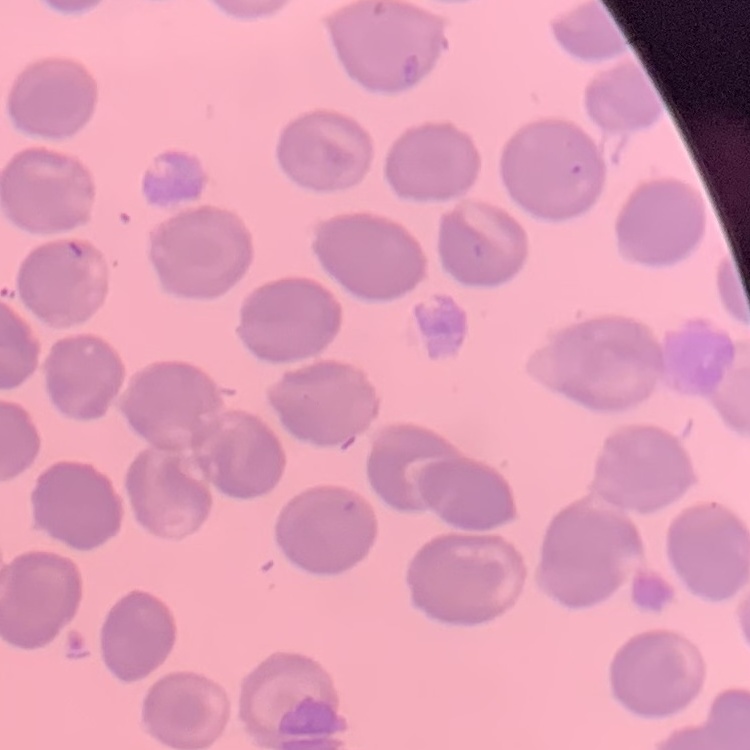

erythrocyte morphology = no rouleaux formation
preparation = thin peripheral smear
stain = Field's or Giemsa
image type = square crop of a larger photomicrograph